Locate every uninfected red blood cell.
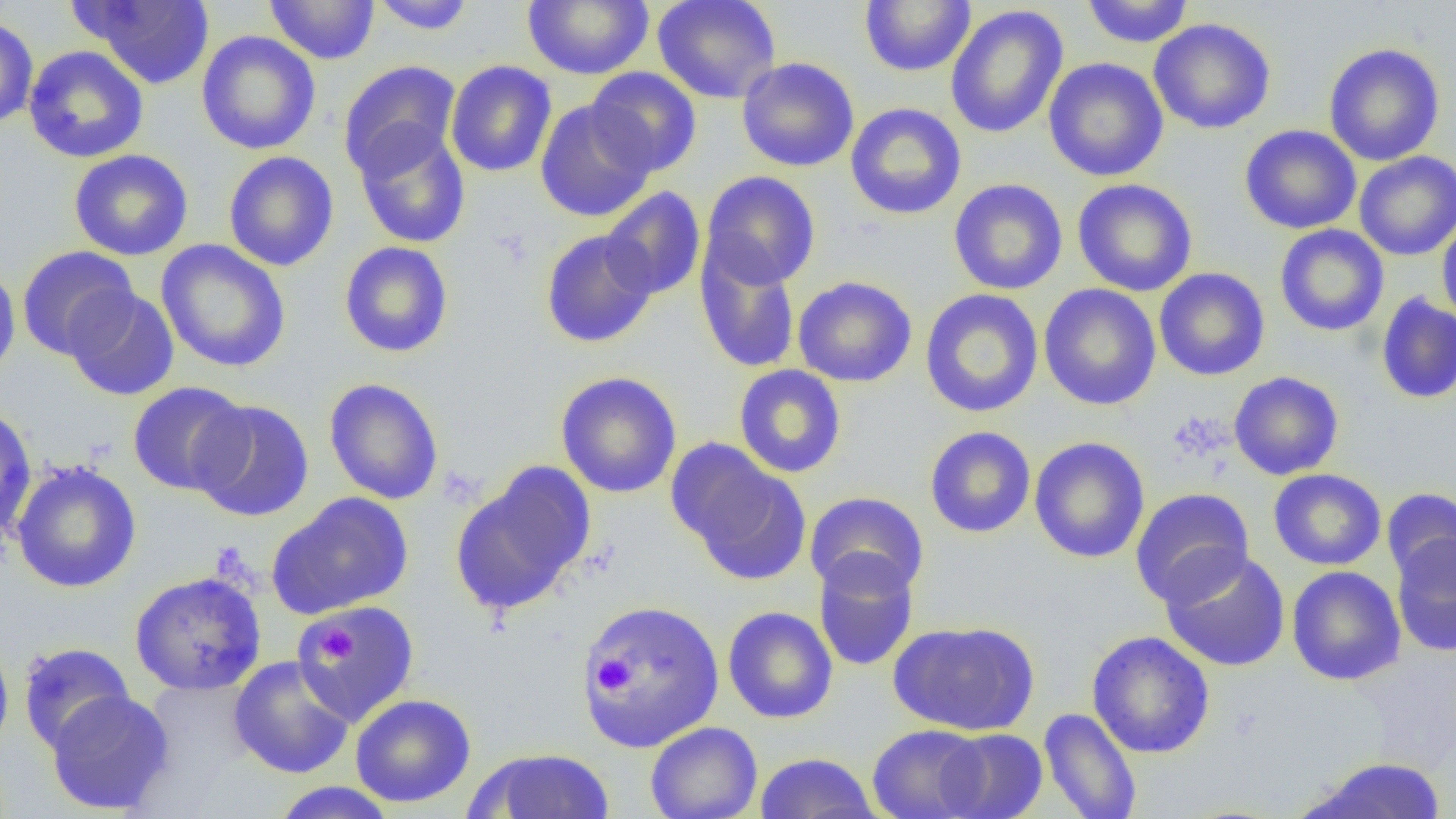

Approximate bounding boxes as (x1,y1)-(x2,y2) corner pairs in pixels.
Uninfected red blood cells: (72,0)-(216,89), (264,0)-(380,65), (368,0)-(477,35), (522,0)-(654,80), (652,0)-(781,104), (859,0)-(976,77), (1081,0)-(1194,48), (944,5)-(1069,139), (0,15)-(38,131), (1149,17)-(1276,134), (196,30)-(321,155), (1323,43)-(1445,166), (23,45)-(149,163), (736,57)-(859,172), (1043,57)-(1169,182), (339,60)-(461,179), (445,60)-(557,177), (585,67)-(701,178), (535,99)-(655,223), (845,102)-(967,220), (353,123)-(471,250), (1239,125)-(1361,234), (68,149)-(194,261), (223,151)-(338,272), (1354,151)-(1456,261), (701,171)-(821,290), (949,178)-(1068,295), (1071,178)-(1198,297), (601,187)-(706,300), (1436,215)-(1456,328), (1274,224)-(1389,337), (540,229)-(659,348), (155,240)-(291,373), (338,241)-(454,358), (695,243)-(802,374), (16,245)-(139,361), (0,264)-(21,380), (1154,267)-(1270,381), (792,275)-(918,388), (1039,284)-(1161,411), (64,287)-(180,401), (919,289)-(1044,418), (1376,293)-(1456,405), (733,365)-(846,478), (555,371)-(682,498), (1228,371)-(1344,480), (324,378)-(444,505), (127,381)-(250,495), (190,399)-(315,522), (0,403)-(37,542), (924,426)-(1036,539), (1029,436)-(1150,564), (668,442)-(810,585), (11,461)-(142,593), (449,464)-(596,617), (1268,469)-(1386,571), (1382,487)-(1456,588), (1130,488)-(1254,608), (804,491)-(929,598), (267,492)-(414,619), (1391,533)-(1456,657), (1160,549)-(1291,671), (813,550)-(920,672), (1286,566)-(1406,686), (129,570)-(267,696), (579,599)-(725,753), (293,600)-(421,727), (722,606)-(838,724), (889,620)-(1039,736), (1086,630)-(1215,759), (0,633)-(14,759), (18,642)-(135,753), (229,655)-(355,779), (45,690)-(175,815), (350,693)-(476,808), (1038,708)-(1142,819), (645,721)-(762,819), (866,724)-(990,819), (936,728)-(1048,819), (467,747)-(616,819), (755,751)-(879,818), (1301,757)-(1448,818), (269,781)-(399,818).

slide-level diagnosis = no evidence of blood parasites
magnification = 1000x
field of view = single
preparation = thin blood film
image size = 1456×819 pixels
modality = optical microscopy
platelet locations = approximate bounding boxes as (x1,y1)-(x2,y2) corner pairs in pixels: (318,627)-(355,662), (594,655)-(635,693)